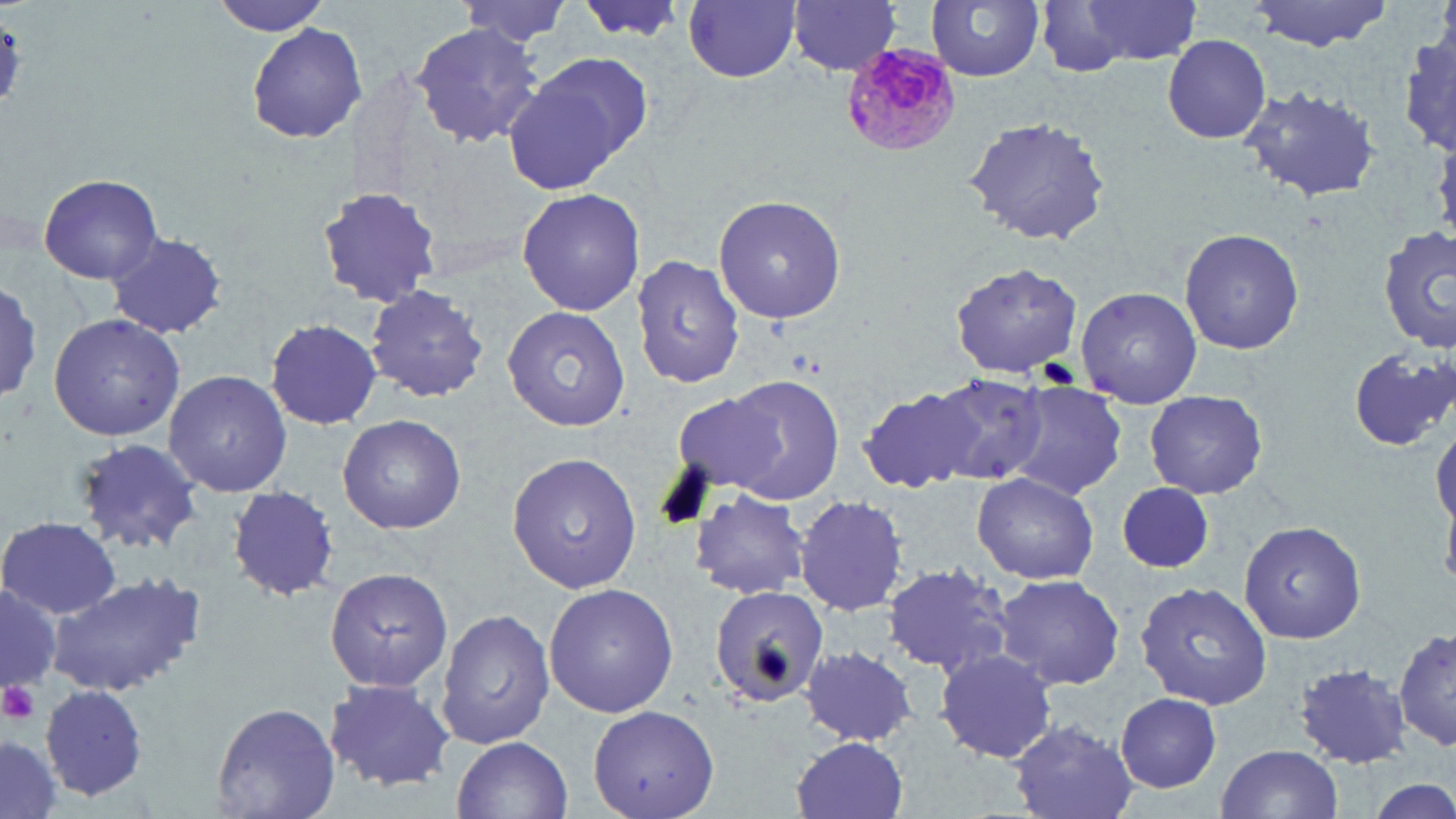
Summary:
  - Coordinate format: approximate bounding boxes as [x1, y1, x2, y2] in pixels
  - Plasmodium malariae-infected red blood cell locations: [845, 42, 961, 153]
  - Uninfected red blood cell locations: [209, 0, 335, 36], [461, 0, 575, 49], [570, 0, 688, 47], [683, 0, 802, 84], [787, 0, 902, 77], [1247, 0, 1397, 50], [928, 1, 1046, 81], [1065, 1, 1206, 67], [1035, 2, 1132, 77], [410, 22, 547, 149], [0, 23, 24, 112], [247, 24, 368, 144], [1402, 30, 1456, 155], [1161, 33, 1272, 145], [511, 52, 657, 187], [1240, 85, 1385, 204], [963, 113, 1114, 246], [38, 173, 163, 285], [314, 185, 444, 310], [516, 187, 646, 318], [712, 193, 847, 323], [1179, 228, 1306, 357], [1379, 228, 1456, 355], [106, 232, 226, 339], [631, 253, 745, 391], [949, 260, 1085, 381], [366, 284, 489, 404], [1, 285, 44, 399], [1076, 286, 1203, 405], [502, 305, 630, 430], [47, 313, 187, 441], [263, 319, 382, 428], [1347, 346, 1456, 452], [164, 369, 292, 498], [926, 371, 1053, 488], [717, 375, 846, 504], [1003, 384, 1128, 501], [856, 385, 986, 495], [672, 389, 789, 497], [1143, 392, 1268, 500], [338, 415, 466, 535], [1432, 418, 1456, 536], [70, 438, 205, 555], [506, 452, 642, 594], [971, 472, 1098, 584], [1115, 481, 1222, 575], [227, 487, 338, 601], [690, 489, 810, 600], [795, 497, 908, 615], [1, 514, 120, 618], [1239, 519, 1367, 643], [882, 562, 1015, 679], [325, 568, 455, 692], [47, 571, 209, 697], [992, 573, 1127, 691], [0, 578, 60, 701], [1135, 580, 1275, 710], [543, 582, 679, 719], [709, 586, 830, 709], [438, 606, 555, 751], [1395, 628, 1454, 755], [801, 647, 918, 747], [933, 648, 1060, 765], [1293, 661, 1414, 768], [321, 677, 456, 792], [40, 684, 149, 800], [1112, 693, 1225, 792], [211, 700, 339, 819], [586, 703, 721, 818], [1008, 720, 1137, 818], [789, 735, 911, 819], [451, 736, 572, 819], [0, 738, 61, 819], [1214, 744, 1344, 819], [1365, 775, 1454, 819]
  - Platelet locations: [0, 680, 41, 727]
  - Slide-level diagnosis: Plasmodium malariae
  - Stain: May-Grünwald-Giemsa
  - Image size: 1456×819 pixels
  - Field of view: one of a larger specimen
  - Preparation: thin blood smear
  - Magnification: 1000x
  - Modality: optical microscopy